Look for Plasmodium parasites.
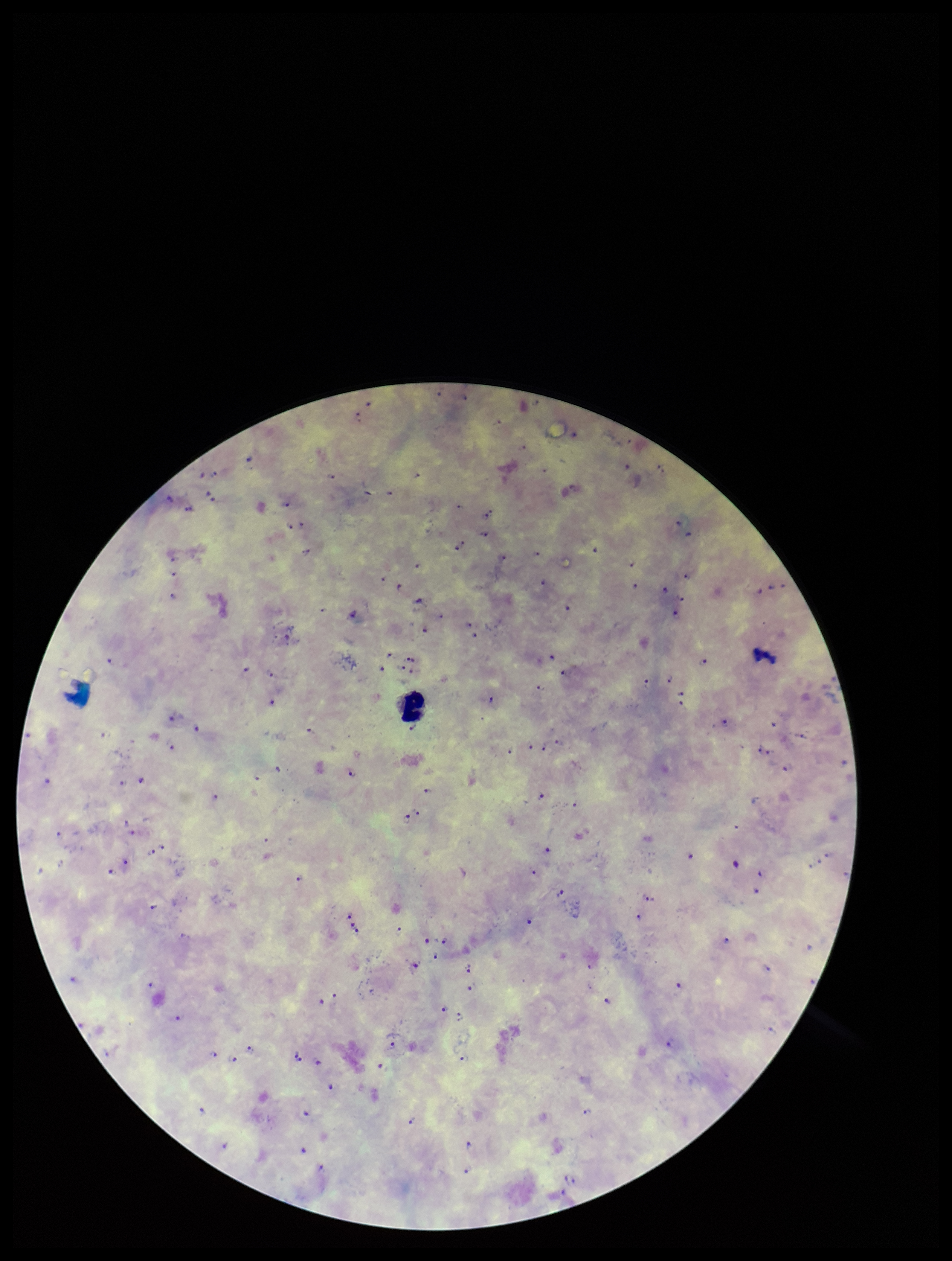
Seen.

Summary:
  - Parasite count: 100
  - Field of view: one from this slide
  - Stain: Giemsa
  - Leukocyte count: 1
  - Image size: 952×1261 pixels
  - Patient malaria status: infected
  - Capture: smartphone photograph through the microscope eyepiece
  - Species reported for this patient: Plasmodium falciparum
  - Preparation: thick